Comment on the morphology of the red blood cells.
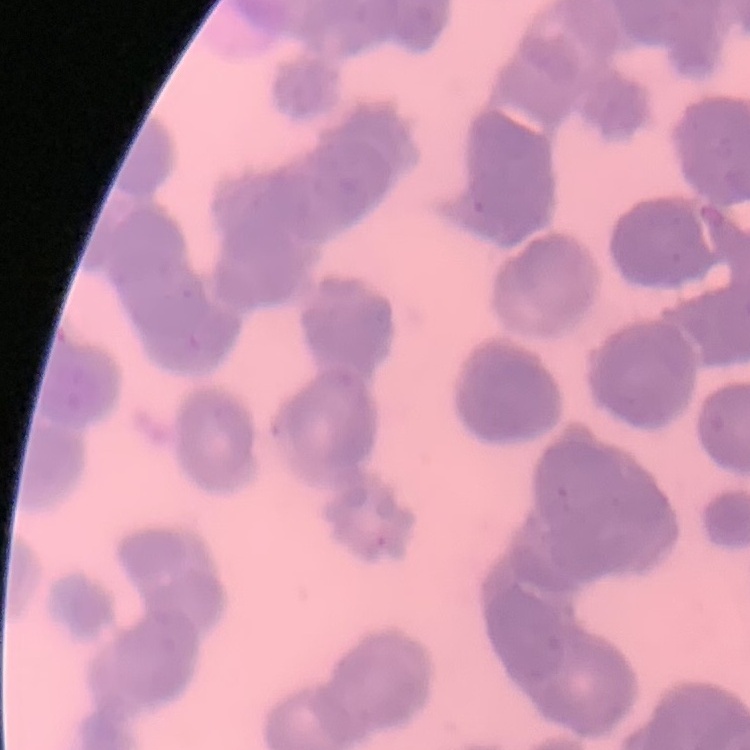

They show rouleaux formation.

Thin blood film. Stained with either Field's or Giemsa. One tile cut from a larger photomicrograph.